Give the extent of all Plasmodium falciparum-infected red blood cells.
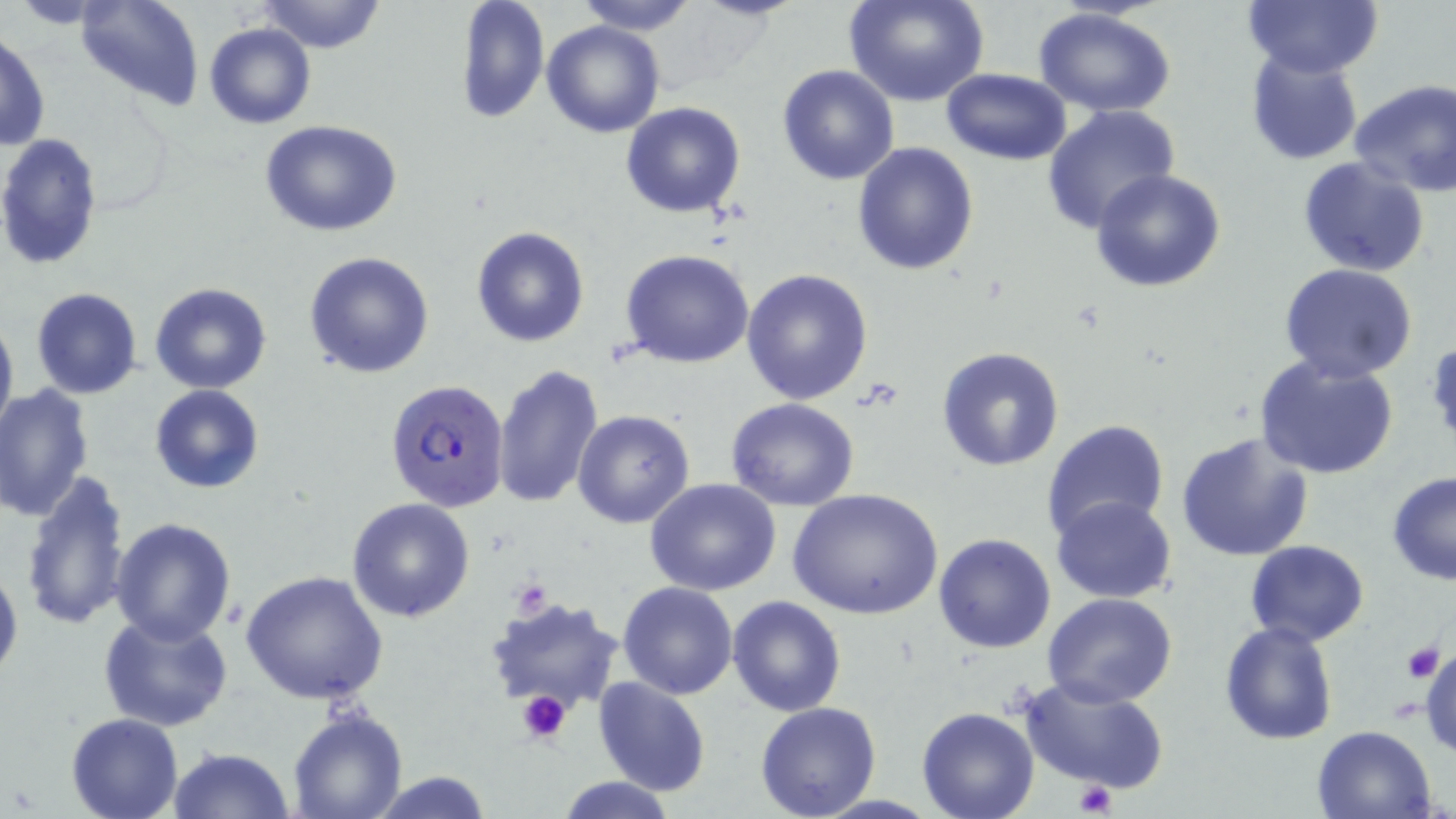

Approximate bounding boxes as (x1, y1, x2, y2) in pixels.
Plasmodium falciparum-infected red blood cells: (384, 379, 510, 513).

Uninfected red blood cell locations: (74, 0, 205, 111), (258, 0, 386, 54), (453, 0, 550, 124), (573, 0, 700, 35), (846, 0, 990, 107), (1241, 0, 1384, 77), (1033, 7, 1177, 115), (541, 21, 665, 138), (204, 22, 316, 130), (0, 31, 49, 152), (1246, 51, 1364, 164), (777, 64, 900, 185), (941, 69, 1071, 164), (1350, 78, 1456, 195), (622, 102, 746, 218), (1042, 104, 1180, 233), (259, 120, 404, 237), (0, 132, 104, 271), (852, 143, 979, 275), (1298, 157, 1431, 276), (1090, 169, 1229, 293), (471, 226, 591, 348), (621, 249, 755, 368), (303, 250, 435, 380), (1279, 264, 1419, 383), (741, 269, 874, 404), (150, 282, 272, 394), (30, 288, 142, 399), (0, 310, 17, 439), (935, 346, 1065, 471), (1252, 353, 1400, 479), (491, 363, 604, 509), (0, 384, 94, 522), (150, 384, 263, 494), (724, 398, 860, 511), (572, 410, 694, 529), (1040, 418, 1168, 543), (1175, 431, 1316, 560), (18, 468, 132, 633), (1387, 471, 1456, 586), (645, 477, 782, 597), (786, 487, 943, 620), (1053, 495, 1176, 603), (346, 498, 476, 623), (110, 517, 237, 644), (933, 533, 1057, 654), (1244, 541, 1369, 646), (0, 558, 23, 688), (241, 569, 388, 706), (617, 581, 740, 699), (1043, 594, 1177, 708), (727, 595, 847, 716), (482, 596, 627, 718), (100, 611, 234, 732), (1219, 621, 1337, 745), (1421, 644, 1456, 761), (1017, 674, 1168, 795), (593, 675, 712, 796), (755, 702, 883, 819), (916, 707, 1039, 819), (288, 709, 409, 819), (66, 713, 182, 819), (1311, 724, 1438, 818), (169, 745, 293, 819), (367, 770, 494, 818), (553, 776, 679, 818). Platelet locations: (511, 575, 554, 616), (1399, 640, 1444, 683), (516, 691, 571, 744), (1071, 779, 1117, 816). Slide-level diagnosis: Plasmodium falciparum. 1000x magnification. May-Grünwald-Giemsa-stained preparation. Image is 1456×819 pixels. Optical microscopy. Single field of view. Thin blood smear.